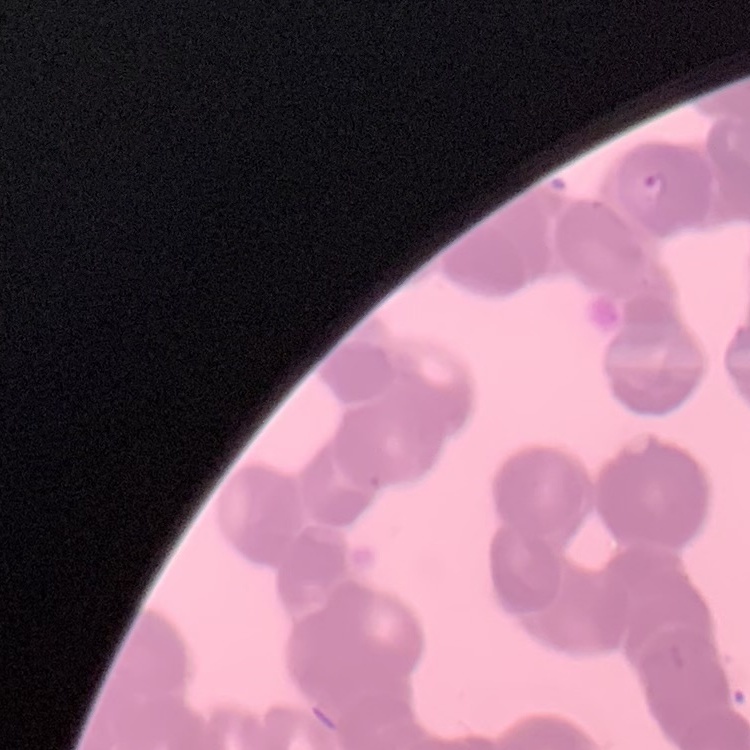

Summary:
  - Erythrocyte morphology: rouleaux formation
  - Image type: square crop of a larger photomicrograph
  - Preparation: thin blood smear
  - Stain: Field's or Giemsa